Describe the morphology of the erythrocytes.
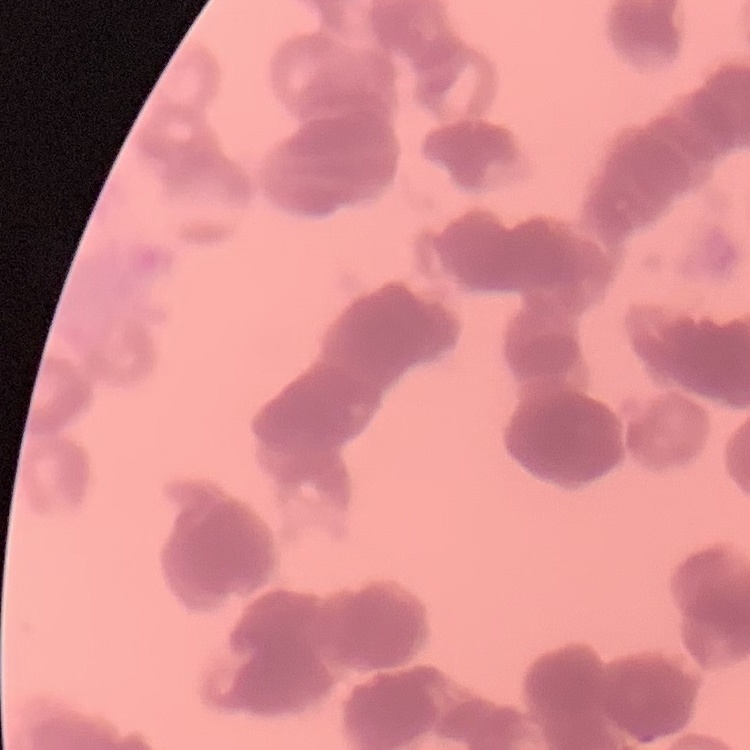
They show rouleaux formation.

stain = Field's or Giemsa
image type = one tile cut from a larger photomicrograph
preparation = thin peripheral smear